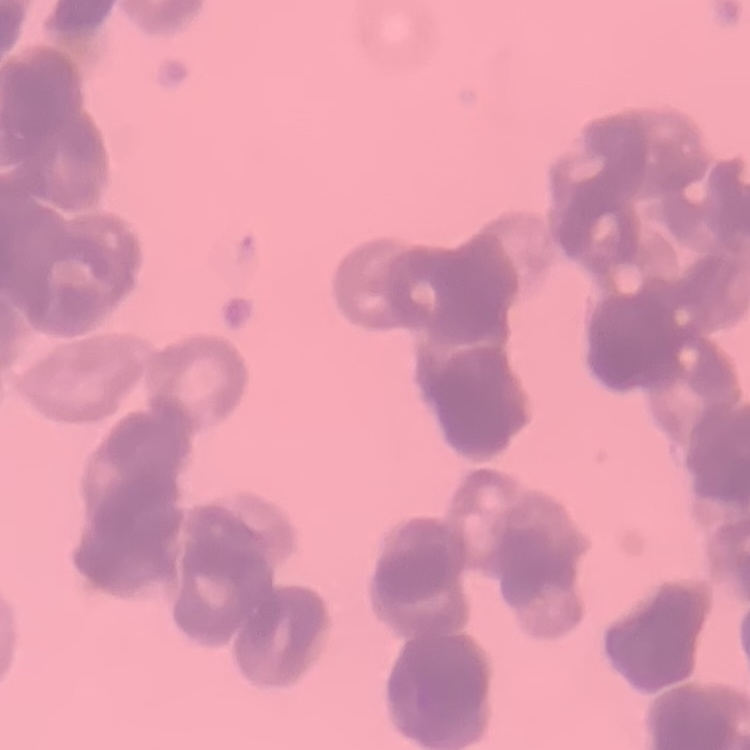

The red blood cells show rouleaux formation. Thin peripheral smear. One tile cut from a larger photomicrograph. Field's or Giemsa stain.